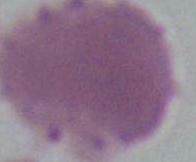

Summary:
  - Magnification: 1000x
  - Identification: erythrocyte
  - Modality: micrograph